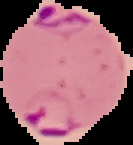 From a thin blood smear. Image is 133×145 pixels. Malaria status: parasitized. Segmented cell region on a black background.